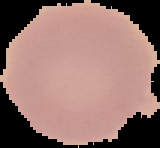 From a thin blood smear. Cell region segmented out of the field of view; the surrounding area is masked to black. Image is 160×148 pixels. Malaria status: uninfected.